State the blood parasite species.
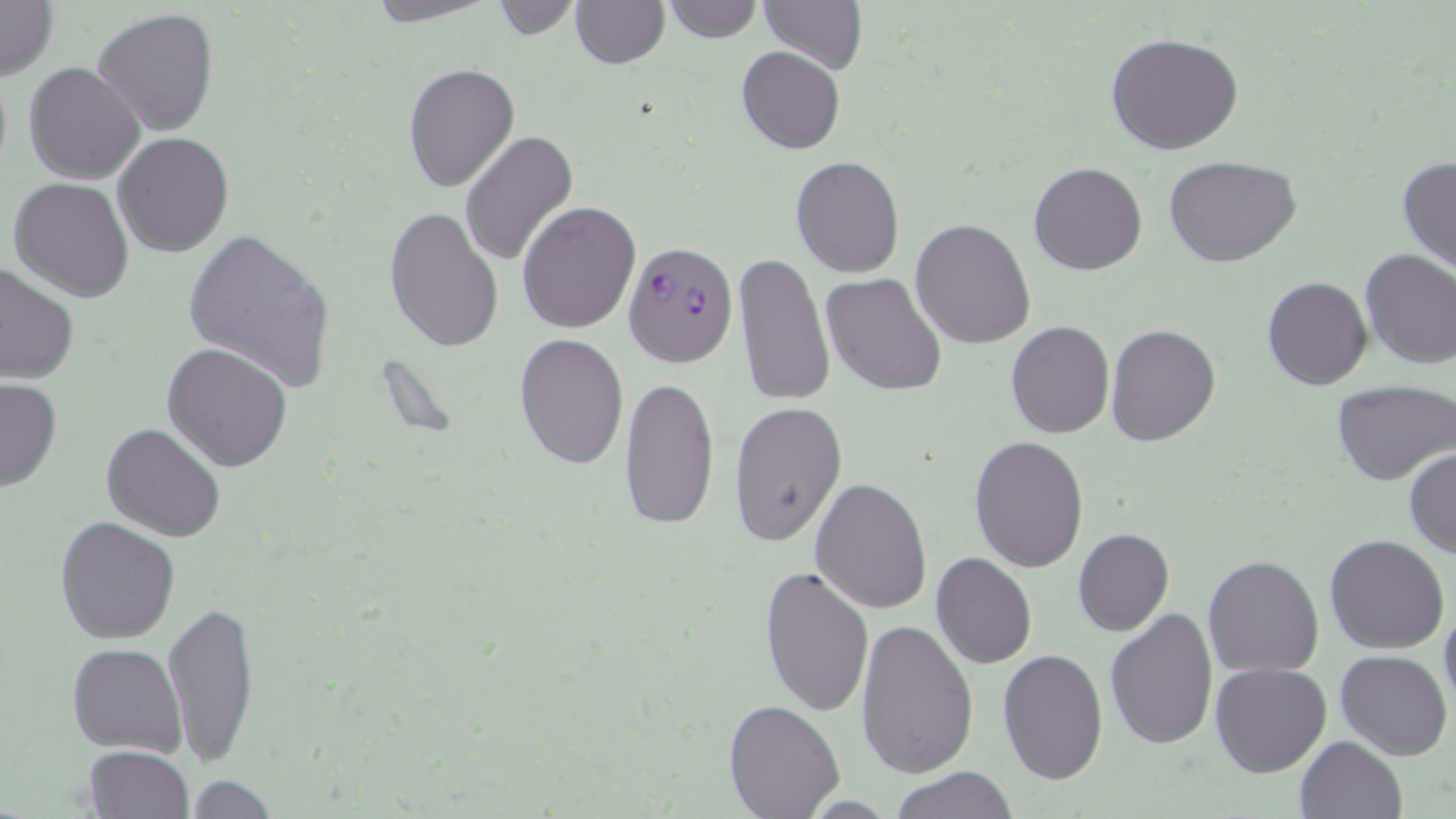

Plasmodium falciparum.

Approximate bounding boxes as (x1, y1, x2, y2) in pixels. Uninfected red blood cell locations: (0, 0, 57, 80), (358, 0, 501, 26), (570, 0, 669, 68), (659, 0, 762, 43), (486, 1, 582, 40), (760, 1, 867, 74), (93, 7, 222, 136), (1104, 32, 1245, 156), (736, 45, 845, 155), (23, 61, 146, 185), (402, 62, 519, 191), (459, 131, 579, 266), (114, 132, 234, 257), (1163, 155, 1303, 268), (1396, 155, 1456, 275), (791, 156, 905, 277), (1029, 162, 1146, 276), (7, 177, 134, 302), (516, 201, 642, 334), (384, 206, 504, 352), (911, 219, 1036, 349), (182, 226, 336, 395), (1359, 248, 1456, 369), (732, 251, 835, 407), (0, 259, 79, 384), (821, 272, 948, 395), (1262, 276, 1373, 390), (1005, 320, 1115, 438), (1105, 323, 1220, 447), (513, 332, 629, 469), (162, 340, 293, 472), (618, 373, 719, 532), (0, 376, 62, 493), (1331, 380, 1455, 487), (730, 401, 847, 548), (101, 422, 225, 542), (968, 436, 1090, 574), (1404, 448, 1456, 559), (810, 478, 932, 614), (55, 517, 180, 644), (1073, 528, 1174, 637), (1325, 535, 1449, 655), (931, 552, 1037, 668), (1203, 554, 1325, 676), (759, 565, 875, 717), (163, 600, 261, 767), (1438, 600, 1456, 715), (1105, 607, 1218, 750), (856, 618, 979, 776), (66, 643, 187, 755), (997, 649, 1108, 782), (1335, 650, 1453, 761), (1208, 661, 1332, 777), (722, 699, 846, 819), (1295, 737, 1407, 819), (84, 746, 193, 818), (890, 766, 1018, 819), (182, 776, 280, 816). Plasmodium falciparum-infected red blood cell locations: (629, 247, 737, 372). Light microscopy. One field of a larger specimen. May-Grünwald-Giemsa-stained preparation. 1000x magnification. Image is 1456×819 pixels. Thin blood smear.